Identify the cell.
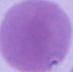
An erythrocyte.

Photomicrograph. Captured at 1000x magnification.